Report the malaria status of this cell.
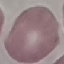
Uninfected.

Photographed with a smartphone camera at the microscope eyepiece. Giemsa-stained preparation. Thin smear of blood. Cell patch, automatically extracted from a larger field of view and resized to 64 × 64 pixels.